Classify this cell by malaria status.
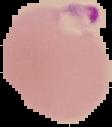
It is parasitized.

{
  "preparation": "thin blood film",
  "image_size": "112×127 pixels",
  "image_type": "segmented cell region with the area outside set to black"
}